Outline each Plasmodium malariae-infected red blood cell.
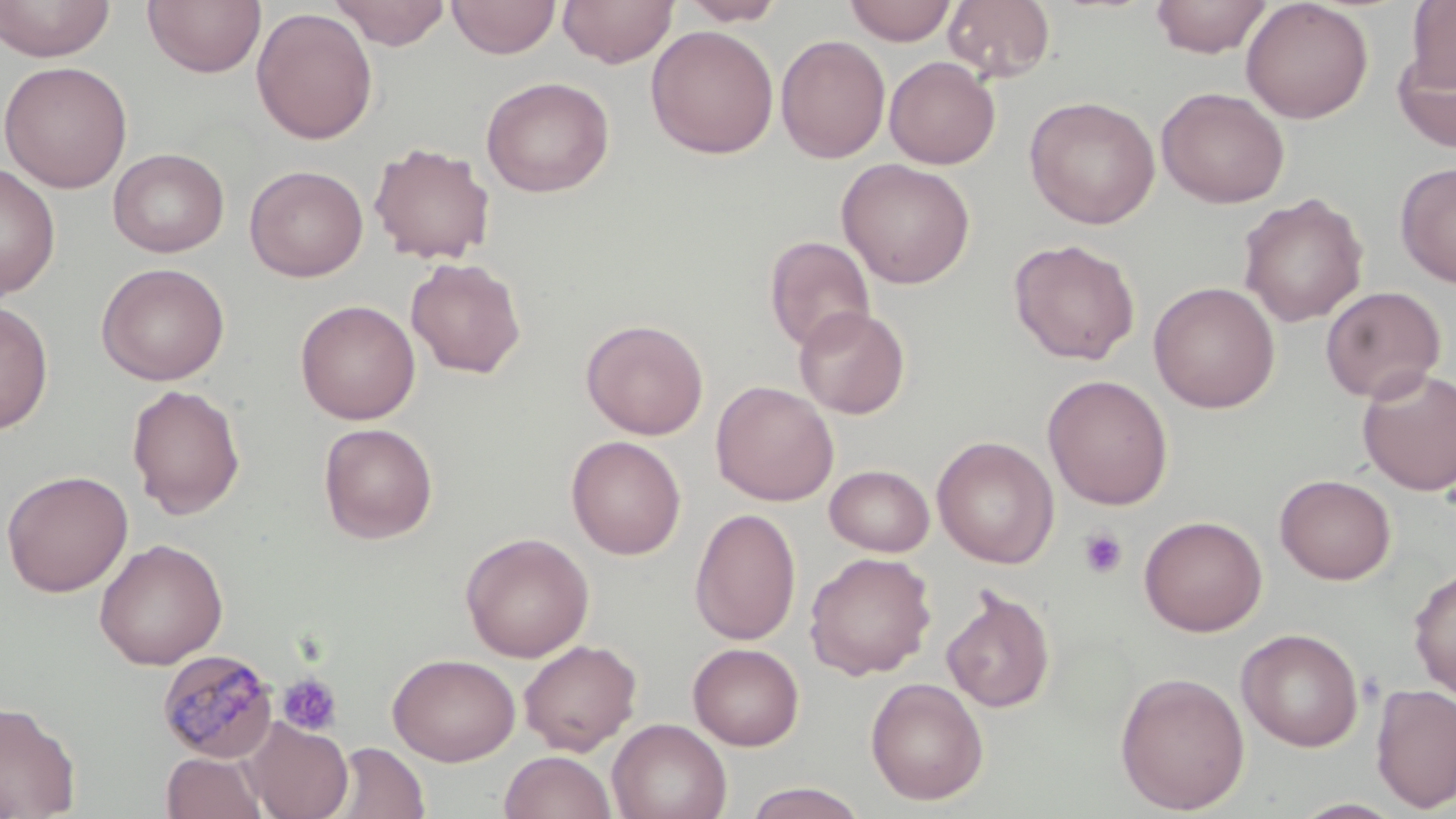
Approximate bounding boxes as (x1,y1)-(x2,y2) corner pairs in pixels.
Plasmodium malariae-infected red blood cells: (157,648)-(279,763).

Summary:
  - Uninfected red blood cell locations: (0,0)-(115,61), (143,0)-(266,79), (447,0)-(560,59), (557,0)-(678,68), (679,0)-(786,26), (844,0)-(956,45), (943,0)-(1056,83), (1150,0)-(1273,58), (1155,0)-(1344,98), (1241,0)-(1373,123), (330,1)-(452,49), (1406,1)-(1456,92), (251,7)-(378,145), (645,25)-(780,159), (775,35)-(891,163), (1392,47)-(1456,153), (884,56)-(1000,169), (0,60)-(133,193), (481,76)-(615,197), (1155,87)-(1290,208), (1024,95)-(1161,229), (368,141)-(496,265), (108,147)-(230,257), (837,158)-(975,289), (0,161)-(60,299), (1395,161)-(1456,288), (245,165)-(368,282), (1238,192)-(1368,328), (764,235)-(876,353), (1008,238)-(1141,365), (405,256)-(527,379), (96,262)-(230,385), (1148,281)-(1280,413), (1320,285)-(1446,404), (295,299)-(421,424), (0,301)-(54,435), (794,305)-(911,419), (581,318)-(709,439), (1356,367)-(1456,496), (1042,374)-(1174,510), (711,380)-(838,506), (125,383)-(246,520), (318,422)-(438,544), (566,435)-(686,560), (932,436)-(1059,568), (824,464)-(935,556), (1,469)-(133,597), (1275,474)-(1396,584), (689,507)-(802,645), (1139,515)-(1267,636), (460,532)-(595,662), (93,538)-(229,670), (804,551)-(937,680), (1409,565)-(1456,700), (941,586)-(1056,713), (1237,628)-(1364,751), (519,638)-(642,755), (688,643)-(804,750), (388,652)-(520,766), (1114,670)-(1251,814), (865,677)-(988,804), (1371,682)-(1456,813), (0,701)-(81,819), (242,718)-(353,819), (608,718)-(731,819), (327,742)-(431,819), (499,750)-(617,819), (162,751)-(267,819), (740,782)-(871,818), (1288,798)-(1410,818)
  - Platelet locations: (1078,528)-(1128,579), (277,672)-(343,737)
  - Slide-level diagnosis: Plasmodium malariae
  - Modality: light microscopy
  - Stain: May-Grünwald-Giemsa
  - Field of view: one of a larger specimen
  - Preparation: thin blood film
  - Magnification: 1000x
  - Image size: 1456×819 pixels